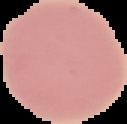

Image is 127×124 pixels. Result: no Plasmodium parasites seen. Cell region segmented out of the field of view; the surrounding area is masked to black. From a thin blood film.